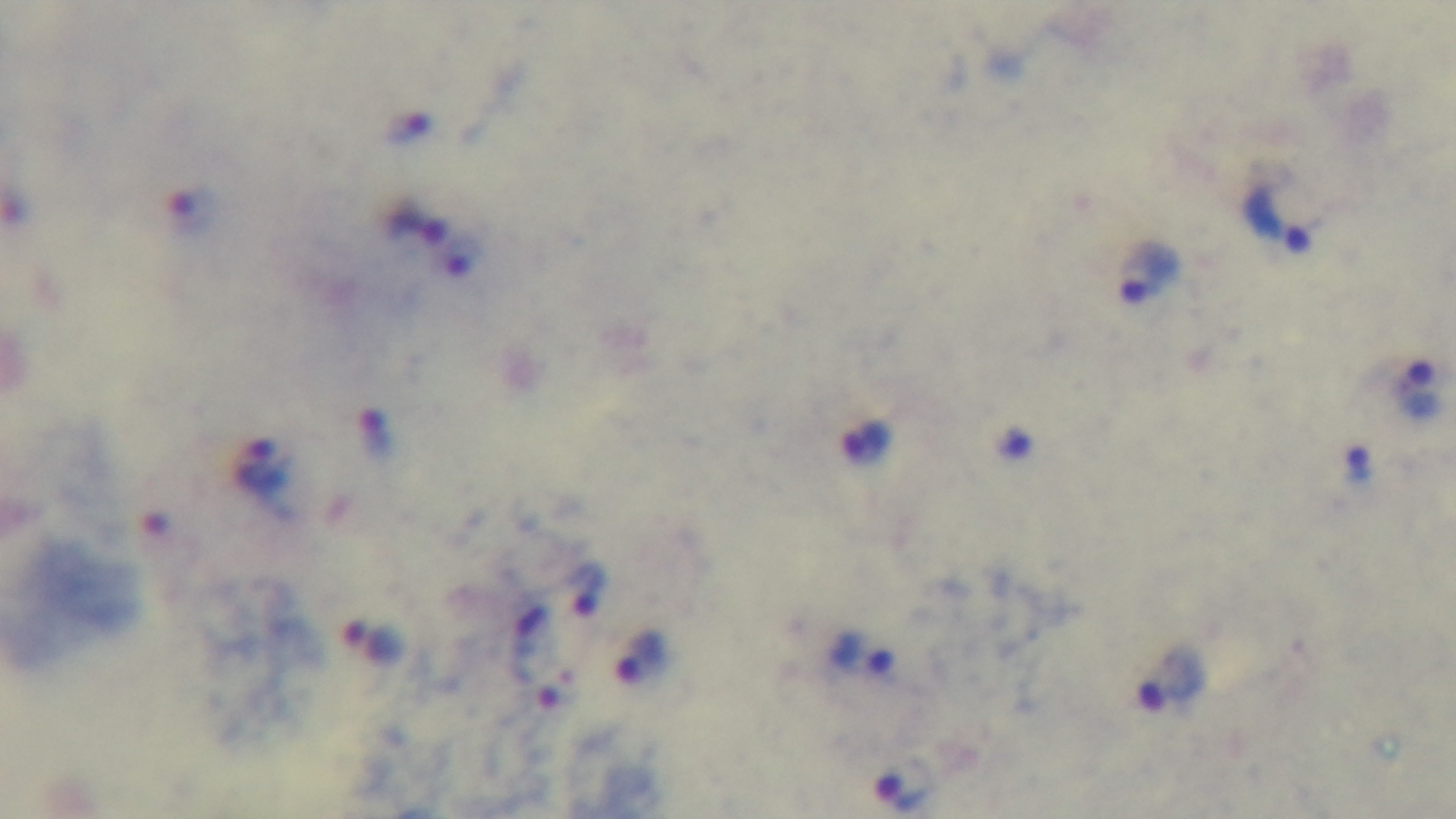
Malaria status: infected. One field from the slide. Mounted 4K digital camera. Photomicrograph. Preparation: thick. 100x oil-immersion objective. Giemsa-stained.